Classify this cell by malaria status.
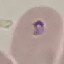
It is parasitized.

Acquired by smartphone through the microscope eyepiece. Thin blood smear. Automatically extracted cell patch, resized to 64 × 64 pixels. Giemsa-stained preparation.